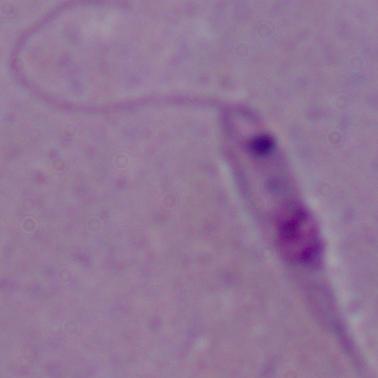 Photomicrograph. A Leishmania parasite is seen. 1000x magnification.